Describe the morphology of the red blood cells.
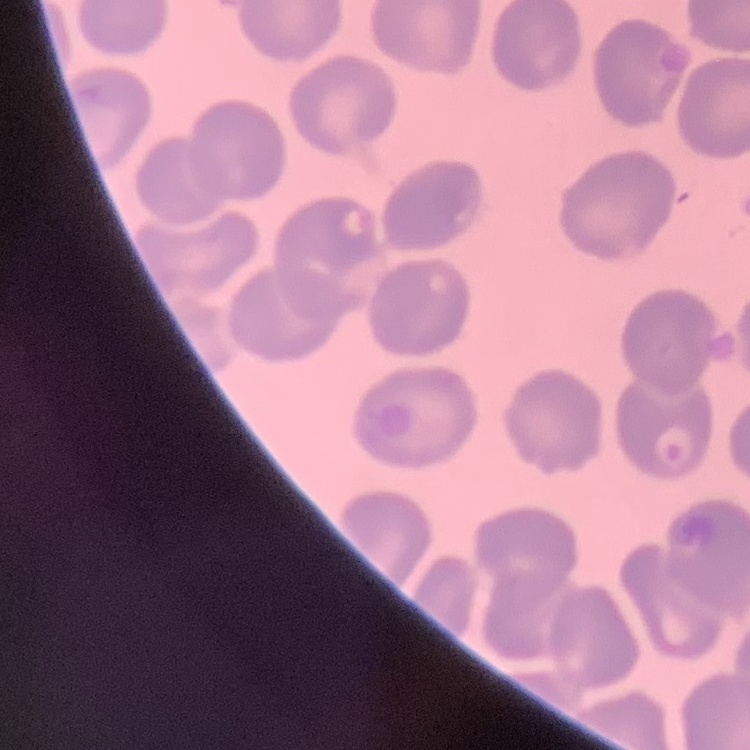

They show no rouleaux formation.

Summary:
  - Stain: Field's or Giemsa
  - Preparation: thin peripheral smear
  - Image type: square crop of a larger photomicrograph